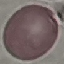

result = no malaria parasites detected
stain = Giemsa
capture = smartphone through the microscope eyepiece
preparation = thin smear
image type = automatically extracted cell patch, resized to 64 × 64 pixels